Comment on the morphology of the erythrocytes.
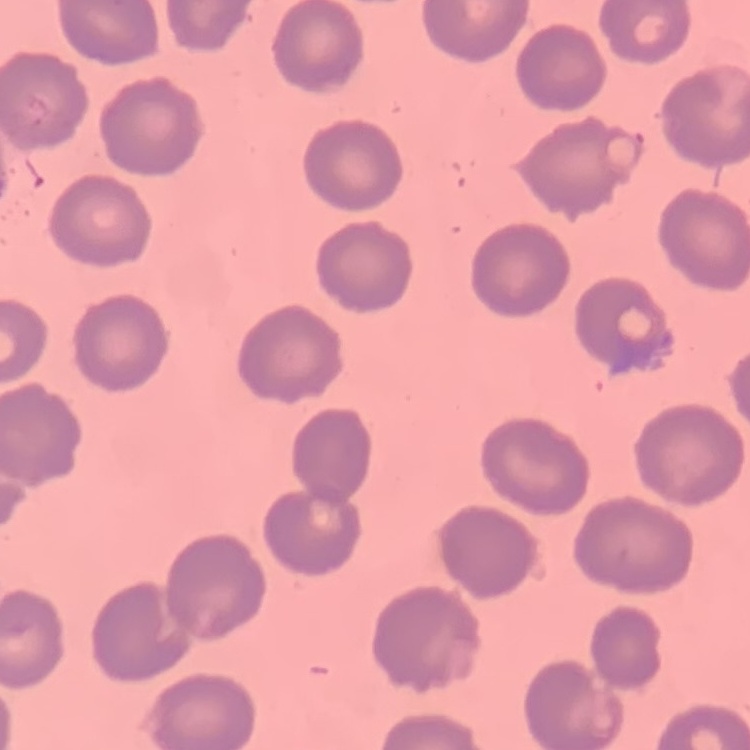

They show no rouleaux formation.

Thin peripheral smear. Stained with either Field's or Giemsa. One tile cut from a larger photomicrograph.